Identify the cell.
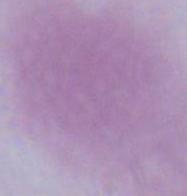

An erythrocyte.

Summary:
  - Modality: micrograph
  - Magnification: 1000x